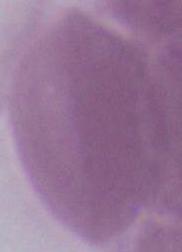

Captured at 1000x magnification. A red blood cell is shown. Micrograph.